Give the extent of all uninfected red blood cells.
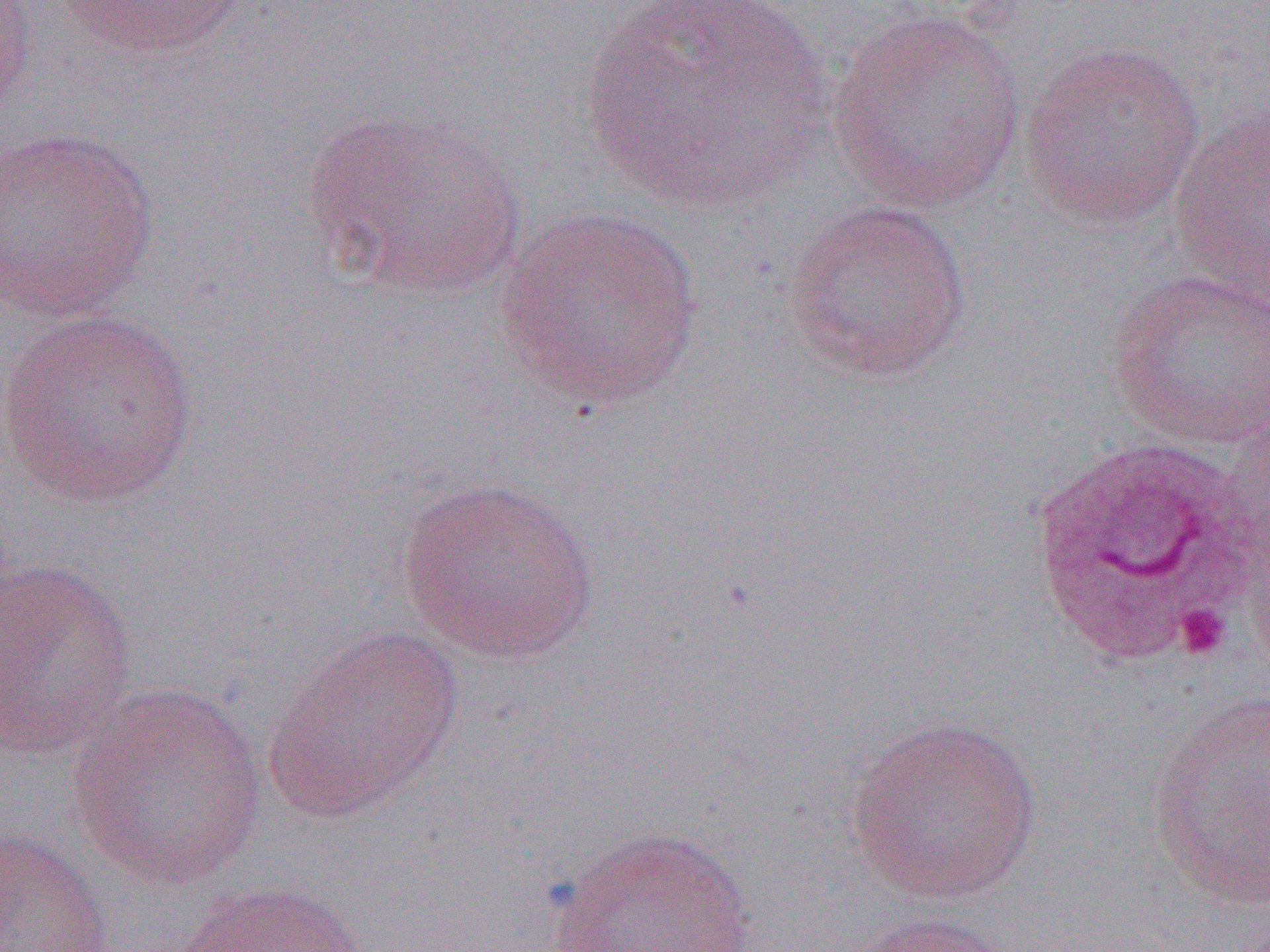

Approximate bounding boxes as (x1,y1)-(x2,y2) corner pairs in pixels.
Uninfected red blood cells: (0,0)-(39,126), (58,0)-(245,63), (574,0)-(835,214), (828,7)-(1027,212), (1017,39)-(1207,230), (304,108)-(526,302), (1167,108)-(1270,308), (0,125)-(161,322), (782,199)-(973,383), (492,206)-(704,412), (1106,268)-(1270,449), (1,306)-(201,508), (1028,436)-(1259,667), (394,475)-(602,666), (1245,521)-(1270,688), (0,555)-(139,761), (263,626)-(465,824), (68,683)-(267,891), (1146,689)-(1270,908), (843,713)-(1043,906), (0,824)-(115,951), (543,826)-(759,951), (173,879)-(370,952), (836,909)-(1026,952).

Platelet locations: (1172,602)-(1232,660). Slide-level diagnosis: Plasmodium ovale. Optical microscopy. Thin blood smear. Single field of view. Image is 1270×952 pixels. Captured at 1000x magnification.